State the preparation type.
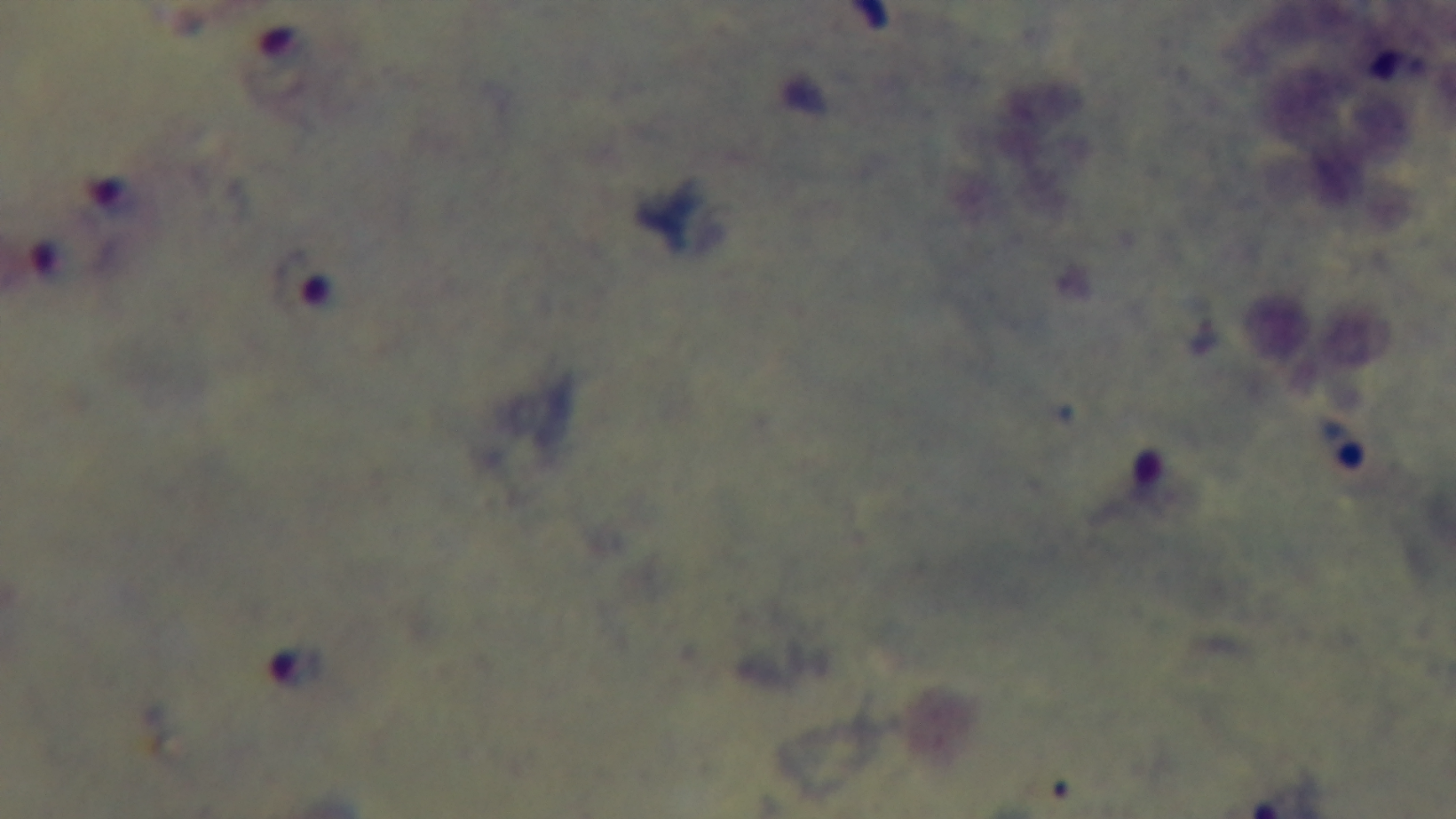
It is a thick blood film.

malaria status = infected
capture = mounted 4K digital camera
stain = Giemsa
objective = 100x oil immersion
modality = light microscopy
field of view = single